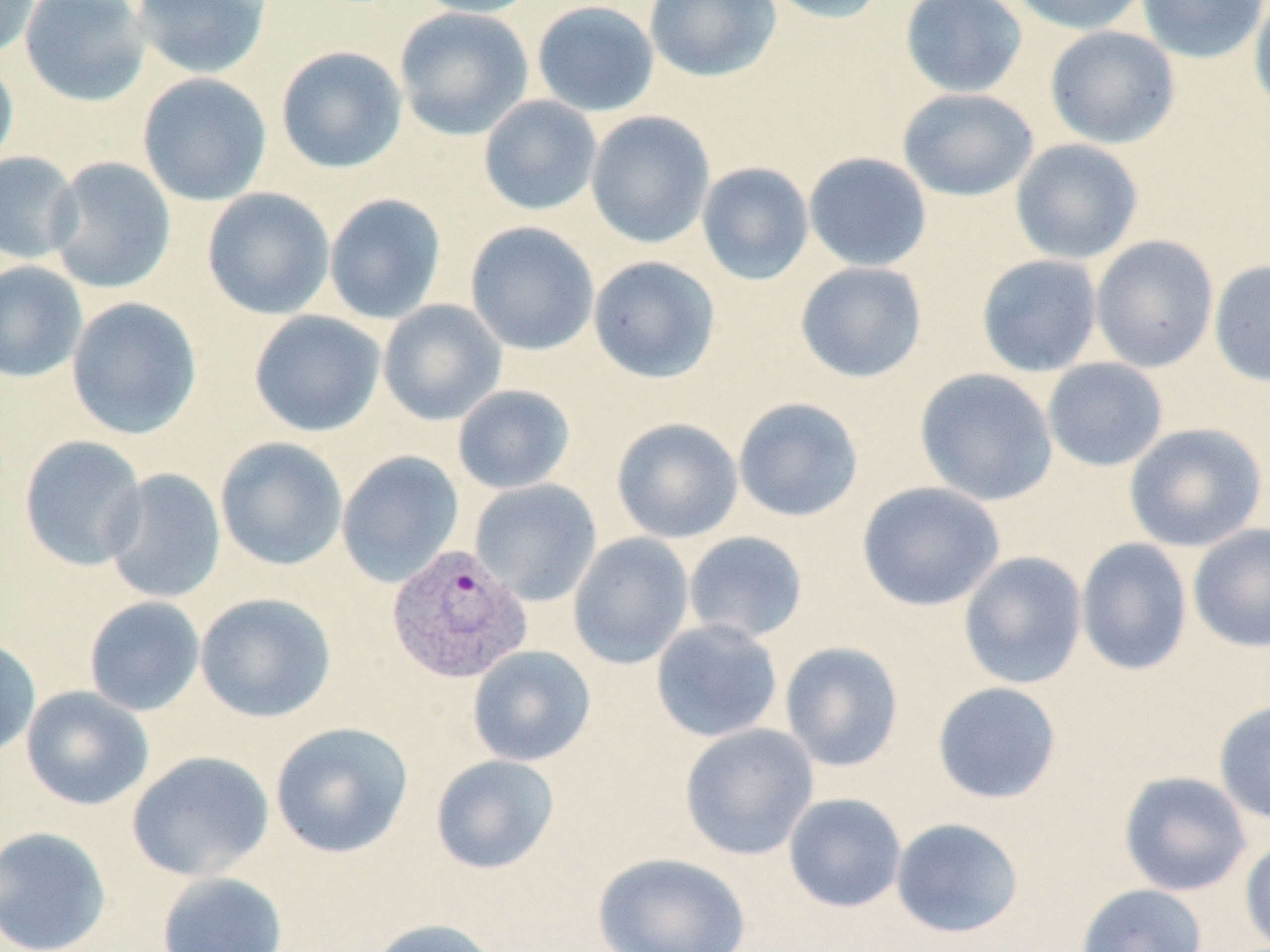

Approximate bounding boxes as [x1, y1, x2, y2] in pixels. Plasmodium vivax-infected red blood cell locations: [386, 543, 532, 684]. Uninfected red blood cell locations: [0, 0, 41, 59], [19, 0, 151, 107], [131, 0, 273, 79], [408, 0, 545, 18], [644, 0, 781, 83], [763, 0, 887, 24], [899, 0, 1028, 99], [1006, 0, 1149, 36], [1137, 0, 1268, 64], [1248, 0, 1270, 121], [531, 1, 660, 117], [393, 7, 534, 141], [1045, 25, 1181, 149], [275, 46, 408, 174], [0, 56, 19, 175], [137, 72, 272, 206], [897, 88, 1039, 202], [478, 95, 603, 216], [586, 111, 715, 249], [1010, 138, 1144, 264], [803, 151, 933, 272], [0, 152, 82, 265], [45, 157, 176, 294], [696, 162, 814, 285], [201, 187, 336, 320], [324, 193, 447, 325], [464, 221, 600, 356], [1090, 234, 1219, 373], [976, 254, 1102, 377], [588, 255, 721, 383], [1209, 259, 1270, 386], [0, 261, 88, 383], [795, 261, 928, 383], [66, 297, 202, 439], [378, 299, 507, 425], [248, 310, 386, 437], [1042, 357, 1168, 472], [914, 367, 1059, 507], [452, 384, 576, 495], [733, 397, 864, 523], [610, 417, 743, 543], [1124, 422, 1267, 552], [19, 436, 148, 571], [215, 437, 348, 571], [336, 451, 465, 587], [103, 468, 226, 604], [469, 479, 602, 606], [856, 481, 1005, 611], [1188, 523, 1270, 653], [683, 531, 809, 644], [568, 532, 694, 668], [1076, 537, 1193, 676], [958, 551, 1088, 690], [195, 592, 337, 723], [83, 596, 205, 716], [651, 618, 783, 742], [0, 637, 42, 761], [779, 641, 905, 772], [467, 645, 596, 767], [932, 681, 1063, 804], [20, 685, 154, 811], [1213, 700, 1270, 824], [270, 721, 414, 859], [679, 723, 819, 860], [126, 750, 274, 882], [430, 754, 561, 875], [1118, 771, 1252, 897], [783, 793, 907, 913], [890, 817, 1024, 938], [0, 826, 113, 952], [1239, 836, 1270, 952], [592, 851, 750, 952], [156, 871, 288, 952], [1076, 883, 1207, 952], [366, 917, 503, 952]. Slide-level diagnosis: Plasmodium vivax. Optical microscopy. Thin blood film. Image is 1270×952 pixels. Captured at 1000x magnification. One field of a larger specimen. May-Grünwald-Giemsa-stained preparation.